Assess the morphology of the red blood cells.
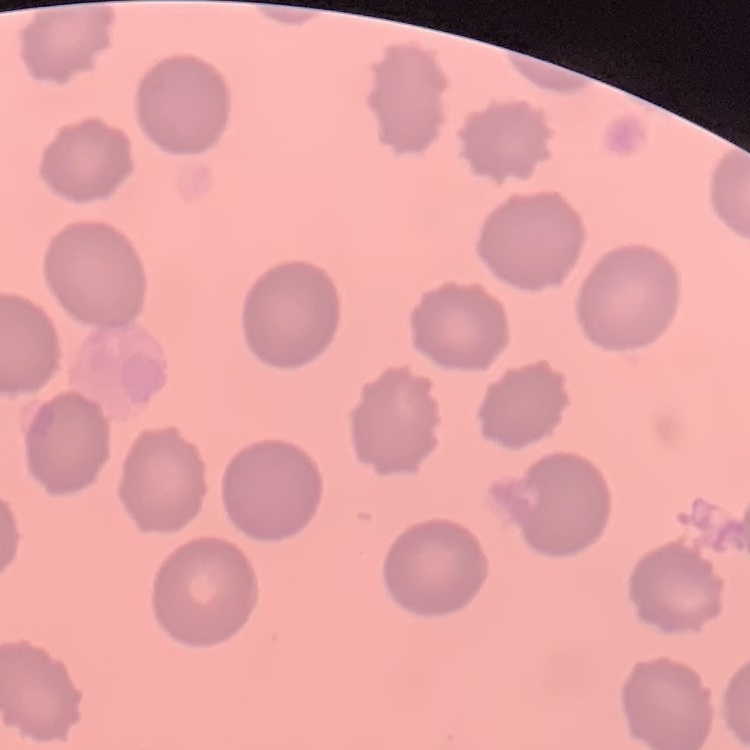
They show no rouleaux formation.

Thin peripheral smear. Stained with either Field's or Giemsa. One tile cut from a larger photomicrograph.